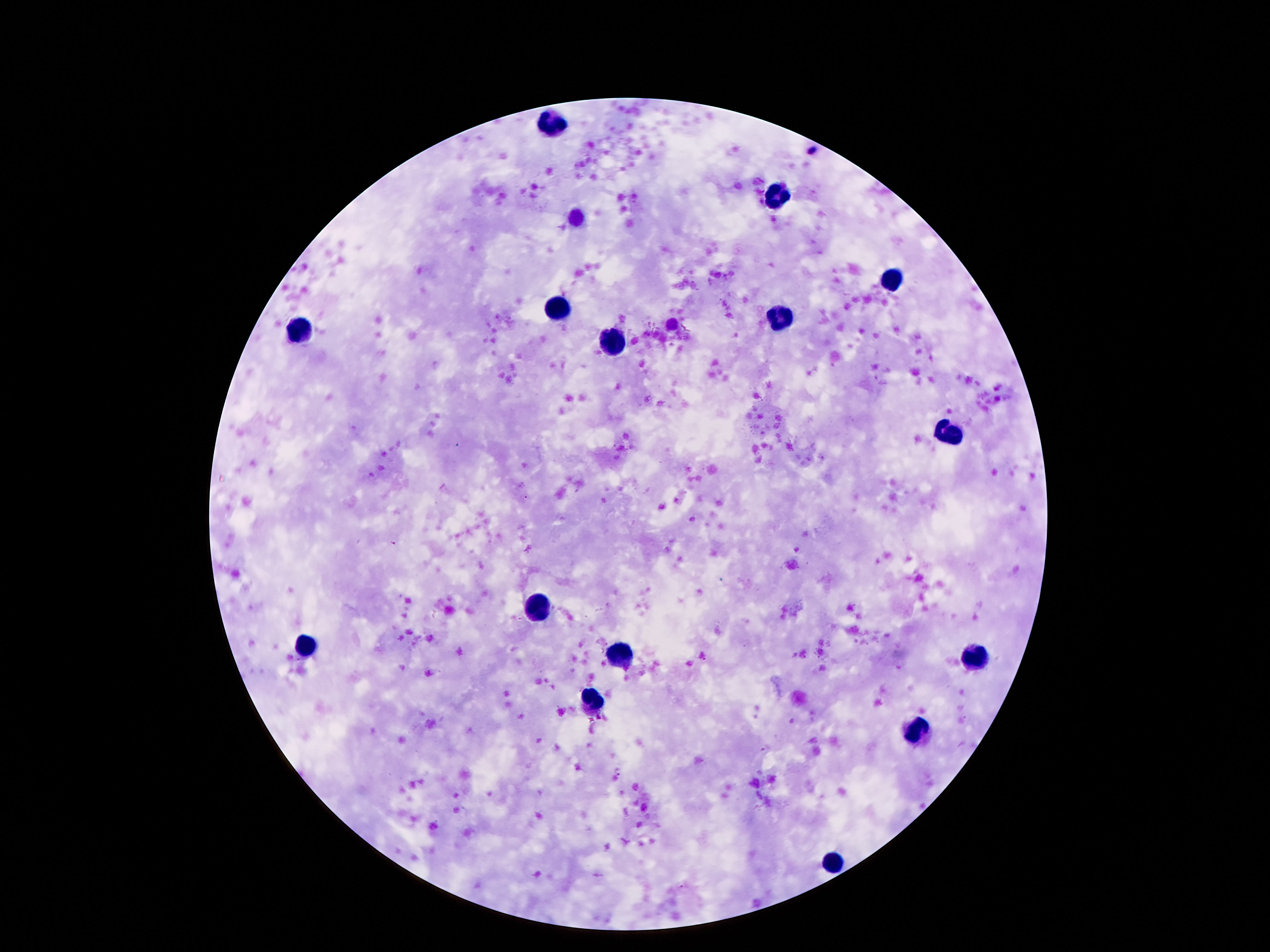

{
  "preparation": "thick blood smear",
  "magnification": "100x",
  "capture": "smartphone camera through the microscope eyepiece",
  "patient_malaria_status": "not infected",
  "stain": "Giemsa",
  "field_of_view": "one from this slide",
  "image_size": "1270×952 pixels",
  "leukocyte_locations": "approximate centers as (x, y) in pixels: (554, 122), (776, 192), (894, 281), (554, 305), (778, 324), (304, 330), (616, 340), (948, 437), (535, 609), (304, 643), (621, 655), (978, 660), (595, 700), (917, 731), (837, 865)"
}